Give a bounding box for every parasitised red blood cell, every trophozoite, every gametocyte, every leukocyte, and every artifact (platelet-like body, stain precipitate, or debris).
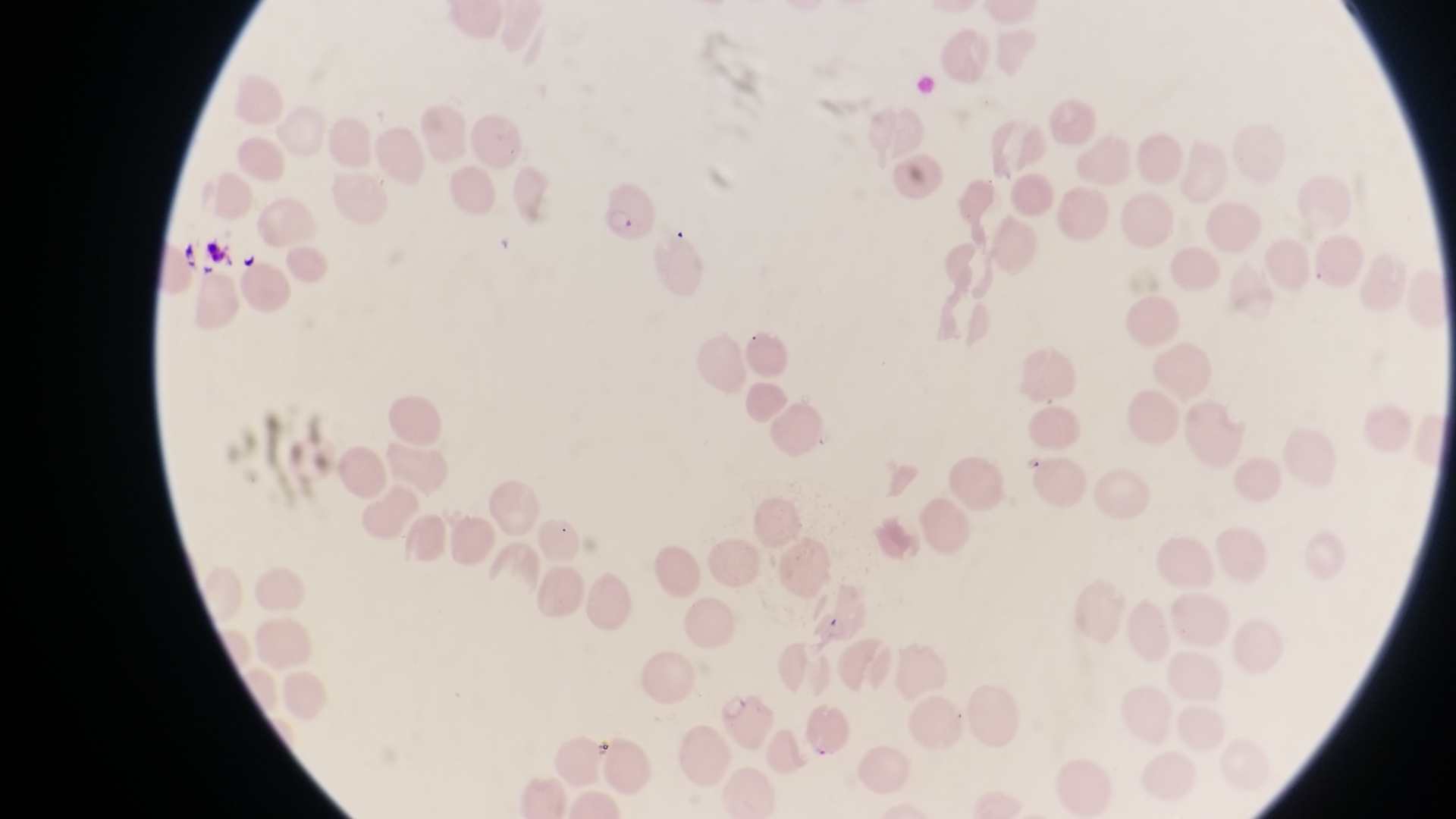
Approximate bounding boxes as {left, top, right, bottom} in pixels.
Parasitised red blood cells: {598, 175, 650, 242}, {714, 692, 775, 752}.
No leukocytes observed.
Artifacts (platelet-like body, stain precipitate, or debris): {201, 231, 243, 271}, {238, 248, 261, 271}, {592, 735, 616, 764}.

At a magnification of 1000x. Single field of view. Image is 1456×819 pixels. Collected in Uganda. Thin blood smear. Photographed through the eyepiece of an Olympus CX-23 microscope with a smartphone camera.